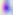
identification = Toxoplasma gondii
magnification = 400x
modality = micrograph